Report the malaria status of this cell.
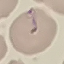
It is uninfected.

Giemsa stain. Thin blood smear. Automatically extracted cell patch, resized to 64 × 64 pixels. Photographed with a smartphone camera at the microscope eyepiece.